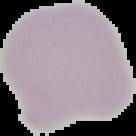

Malaria status: uninfected. From a thin blood film. Image is 136×136 pixels. Segmented cell region on a black background.